Locate platelets.
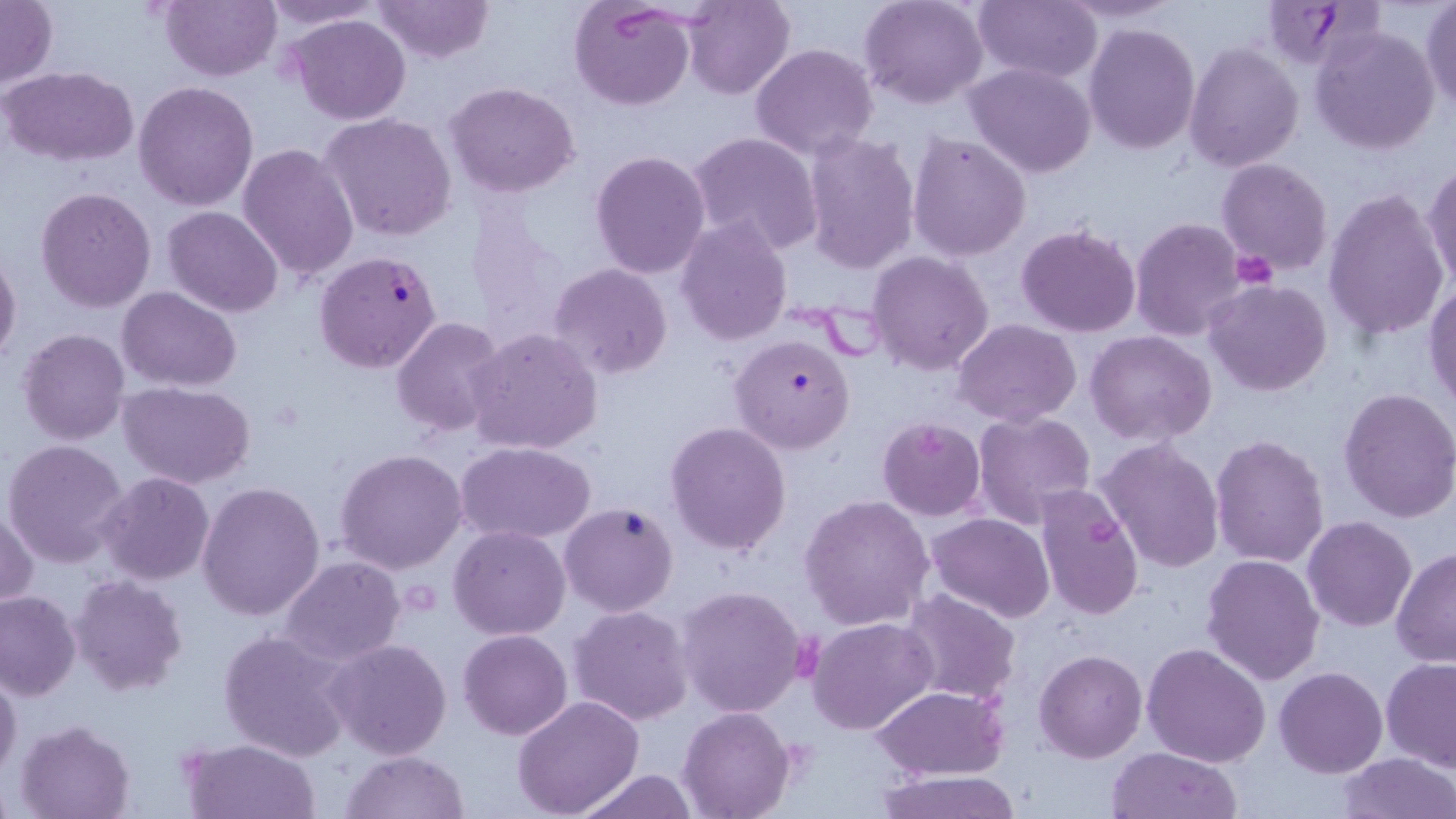
Approximate bounding boxes as (x1,y1)-(x2,y2) corner pairs in pixels.
Platelets: (1229,252)-(1277,290).

slide-level diagnosis = Plasmodium falciparum
field of view = single
stain = May-Grünwald-Giemsa
uninfected red blood cell locations = approximate bounding boxes as (x1,y1)-(x2,y2) corner pairs in pixels: (160,0)-(281,81), (258,0)-(388,32), (372,0)-(493,63), (570,0)-(695,111), (859,0)-(988,109), (974,0)-(1101,81), (1054,0)-(1187,25), (1,1)-(56,87), (681,1)-(794,100), (1420,2)-(1455,113), (287,13)-(413,126), (1083,23)-(1199,154), (1312,28)-(1440,154), (1184,42)-(1304,171), (750,43)-(879,161), (964,62)-(1097,179), (3,66)-(138,166), (134,80)-(258,212), (445,82)-(580,198), (321,114)-(457,242), (687,132)-(823,255), (907,132)-(1032,261), (801,133)-(920,273), (238,144)-(360,283), (590,151)-(711,278), (1217,158)-(1333,276), (1423,165)-(1456,294), (35,187)-(156,312), (1323,188)-(1449,342), (164,206)-(282,315), (676,217)-(792,345), (1130,217)-(1251,339), (1016,223)-(1141,337), (0,250)-(22,366), (868,250)-(996,375), (548,264)-(674,381), (1203,281)-(1332,398), (1424,283)-(1456,412), (117,287)-(242,390), (390,317)-(508,439), (953,318)-(1084,425), (467,327)-(603,455), (19,328)-(129,446), (1085,330)-(1217,445), (119,380)-(257,490), (1337,388)-(1456,524), (972,410)-(1097,531), (877,416)-(986,520), (664,420)-(792,556), (1209,434)-(1329,569), (1096,438)-(1225,574), (3,440)-(130,568), (458,442)-(595,545), (335,449)-(467,575), (99,472)-(214,584), (197,480)-(325,621), (1033,484)-(1145,624), (798,494)-(935,632), (1,506)-(38,608), (927,513)-(1056,622), (1302,516)-(1417,634), (448,526)-(570,640), (1391,545)-(1456,668), (1200,553)-(1325,685), (277,557)-(405,666), (69,574)-(189,697), (676,585)-(808,717), (0,588)-(81,700), (898,589)-(1021,705), (568,604)-(695,726), (808,617)-(937,735), (218,629)-(354,761), (458,630)-(572,740), (325,638)-(453,760), (1141,643)-(1271,768), (1034,647)-(1147,762), (1381,657)-(1456,769), (1274,667)-(1388,778), (0,669)-(23,781), (871,686)-(1011,779), (512,697)-(644,818), (678,705)-(798,818), (15,718)-(136,819), (180,737)-(322,819), (1105,746)-(1242,819), (338,749)-(471,819), (1337,752)-(1455,819), (571,767)-(698,819), (876,770)-(1022,819)
magnification = 1000x
modality = optical microscopy
preparation = thin blood film
image size = 1456×819 pixels
Plasmodium falciparum-infected red blood cell locations = approximate bounding boxes as (x1,y1)-(x2,y2) corner pairs in pixels: (1262,0)-(1374,70), (314,250)-(443,373), (728,333)-(855,455), (559,501)-(680,617)